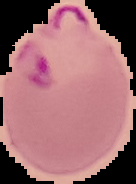
preparation = thin blood smear
image type = segmented cell region with the area outside set to black
image size = 136×184 pixels
result = Plasmodium parasites identified